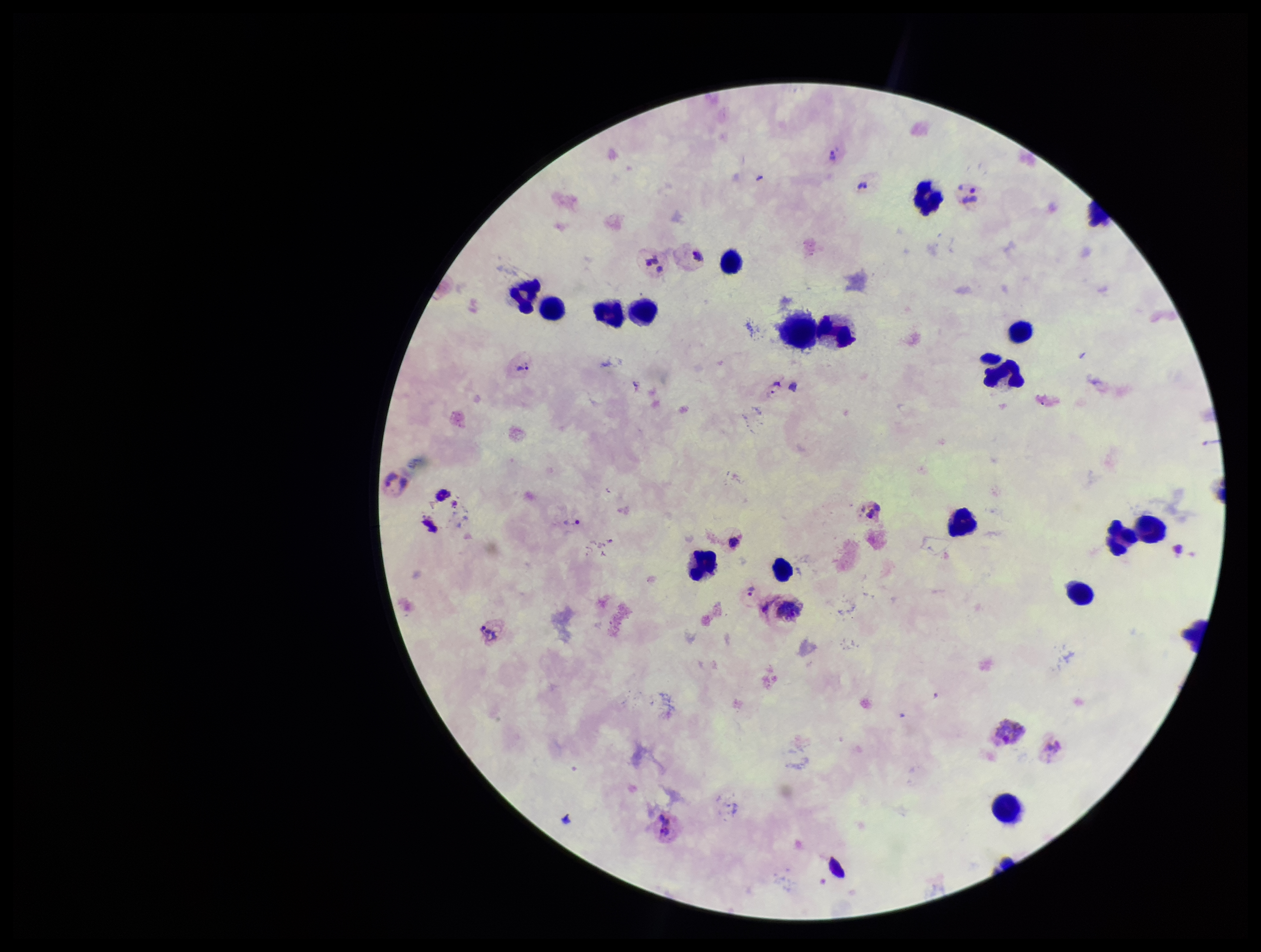

{
  "species_reported_for_this_patient": "Plasmodium vivax",
  "patient_malaria_status": "infected",
  "field_of_view": "one from this slide",
  "preparation": "thick smear",
  "image_size": "1261×952 pixels",
  "leukocyte_count": 20,
  "parasite_count": 5,
  "capture": "smartphone photograph through the microscope eyepiece",
  "plasmodium_parasites": "seen",
  "stain": "Giemsa"
}